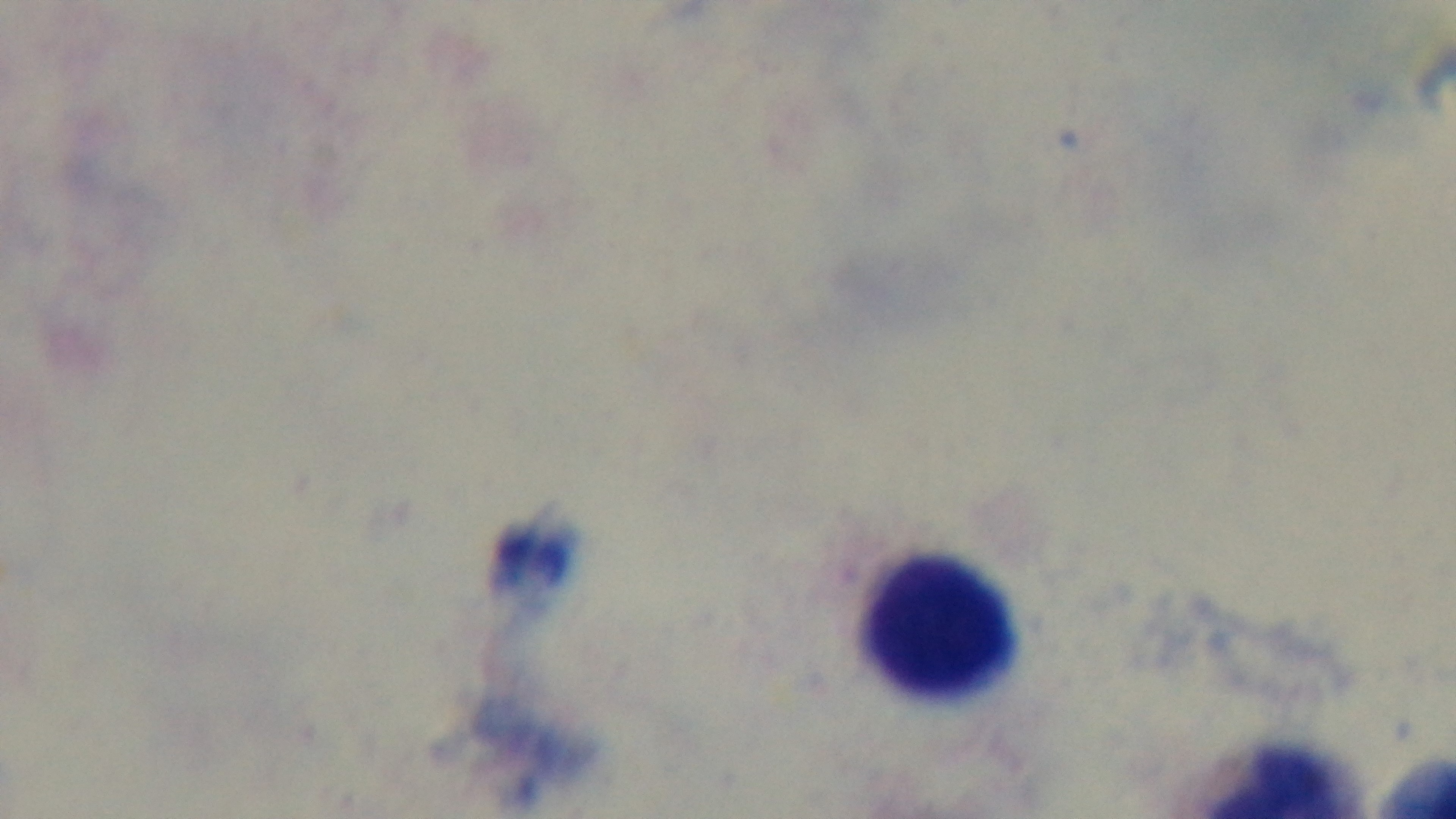

Summary:
  - Stain: Giemsa
  - Preparation: thick blood film
  - Objective: 100x oil immersion
  - Field of view: one from the slide
  - Malaria status: negative
  - Modality: light microscopy
  - Capture: mounted 4K digital camera